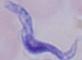

magnification: 1000x
modality: photomicrograph
identification: trypanosome